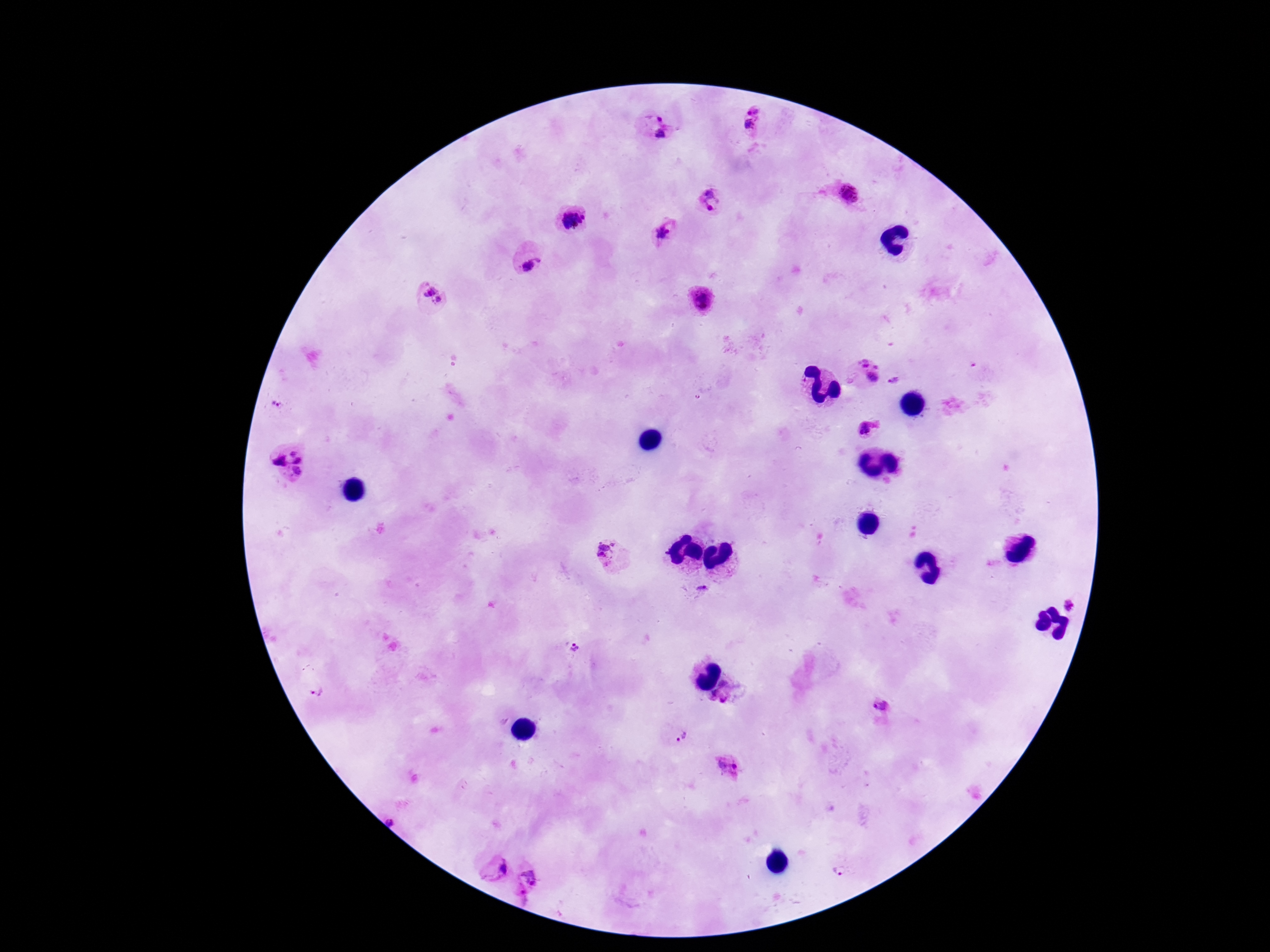

Plasmodium parasite locations = approximate centers as (x, y) in pixels: (754, 109), (659, 116), (750, 125), (661, 134), (707, 193), (850, 194), (709, 208), (573, 221), (663, 233), (532, 266), (429, 290), (439, 300), (701, 302), (866, 373), (897, 382), (274, 405), (869, 429), (287, 463), (608, 553), (700, 587), (1072, 604), (573, 649), (316, 692), (725, 693), (881, 707), (682, 736), (728, 766), (391, 820), (496, 868), (529, 876), (522, 892)
image size = 1270×952 pixels
stain = Giemsa
magnification = 100x
field of view = one from this slide
capture = smartphone camera through the microscope eyepiece
patient malaria status = infected
preparation = thick peripheral-blood smear